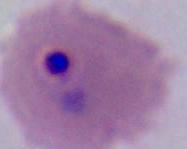
A Plasmodium parasite is shown. Photomicrograph. 400x or 1000x magnification.